Comment on the morphology of the erythrocytes.
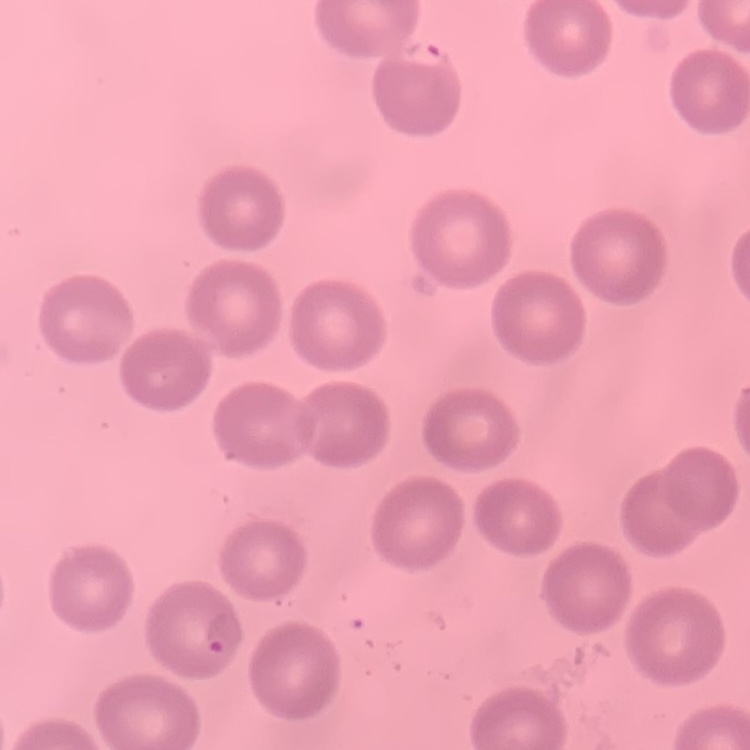

They show no rouleaux formation.

stain = Field's or Giemsa
preparation = thin blood smear
image type = one tile cut from a larger photomicrograph